Locate and identify every blood parasite.
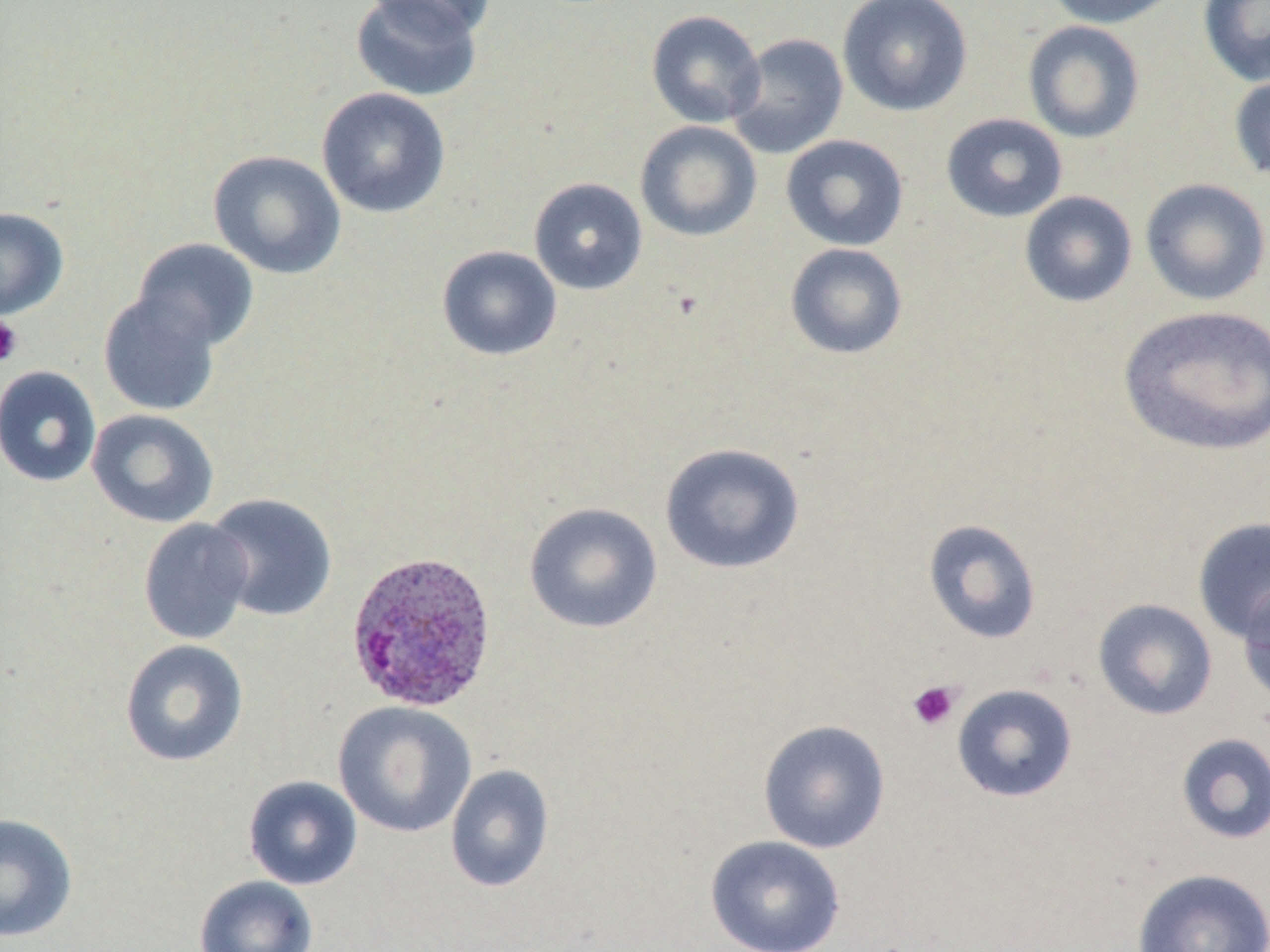

Approximate bounding boxes as named x1/y1/x2/y2 corners in pixels.
Plasmodium ovale-infected red blood cells: (x1=344, y1=549, x2=498, y2=714).
No Plasmodium falciparum, Plasmodium malariae, Plasmodium vivax, Babesia divergens, or Trypanosoma brucei observed.

Platelet locations: (x1=0, y1=315, x2=23, y2=367), (x1=907, y1=680, x2=962, y2=731). Uninfected red blood cell locations: (x1=350, y1=0, x2=483, y2=102), (x1=365, y1=0, x2=496, y2=40), (x1=837, y1=0, x2=973, y2=117), (x1=1045, y1=0, x2=1185, y2=28), (x1=1197, y1=1, x2=1270, y2=88), (x1=646, y1=10, x2=766, y2=128), (x1=1022, y1=20, x2=1146, y2=143), (x1=727, y1=33, x2=849, y2=159), (x1=1227, y1=72, x2=1270, y2=183), (x1=317, y1=87, x2=451, y2=218), (x1=940, y1=113, x2=1068, y2=223), (x1=635, y1=120, x2=762, y2=242), (x1=781, y1=135, x2=909, y2=251), (x1=208, y1=149, x2=346, y2=280), (x1=528, y1=177, x2=648, y2=296), (x1=1139, y1=178, x2=1270, y2=306), (x1=1019, y1=191, x2=1138, y2=308), (x1=0, y1=207, x2=69, y2=320), (x1=132, y1=238, x2=259, y2=351), (x1=784, y1=243, x2=908, y2=360), (x1=437, y1=245, x2=561, y2=361), (x1=98, y1=290, x2=221, y2=416), (x1=1118, y1=305, x2=1270, y2=457), (x1=0, y1=366, x2=101, y2=487), (x1=87, y1=409, x2=219, y2=528), (x1=659, y1=442, x2=806, y2=575), (x1=205, y1=493, x2=337, y2=622), (x1=524, y1=502, x2=662, y2=634), (x1=1192, y1=516, x2=1270, y2=645), (x1=138, y1=518, x2=255, y2=645), (x1=922, y1=518, x2=1042, y2=644), (x1=1237, y1=580, x2=1270, y2=708), (x1=1092, y1=598, x2=1218, y2=721), (x1=120, y1=639, x2=249, y2=767), (x1=951, y1=683, x2=1078, y2=802), (x1=333, y1=701, x2=477, y2=838), (x1=757, y1=719, x2=891, y2=853), (x1=1175, y1=732, x2=1270, y2=845), (x1=445, y1=764, x2=555, y2=892), (x1=243, y1=775, x2=363, y2=890), (x1=0, y1=813, x2=78, y2=942), (x1=705, y1=835, x2=846, y2=952), (x1=1131, y1=867, x2=1270, y2=952), (x1=195, y1=875, x2=319, y2=952). Slide-level diagnosis: Plasmodium ovale. Image is 1270×952 pixels. Optical microscopy. Thin blood film. May-Grünwald-Giemsa stain. 1000x magnification. Single field of view.